Locate and identify every blood parasite.
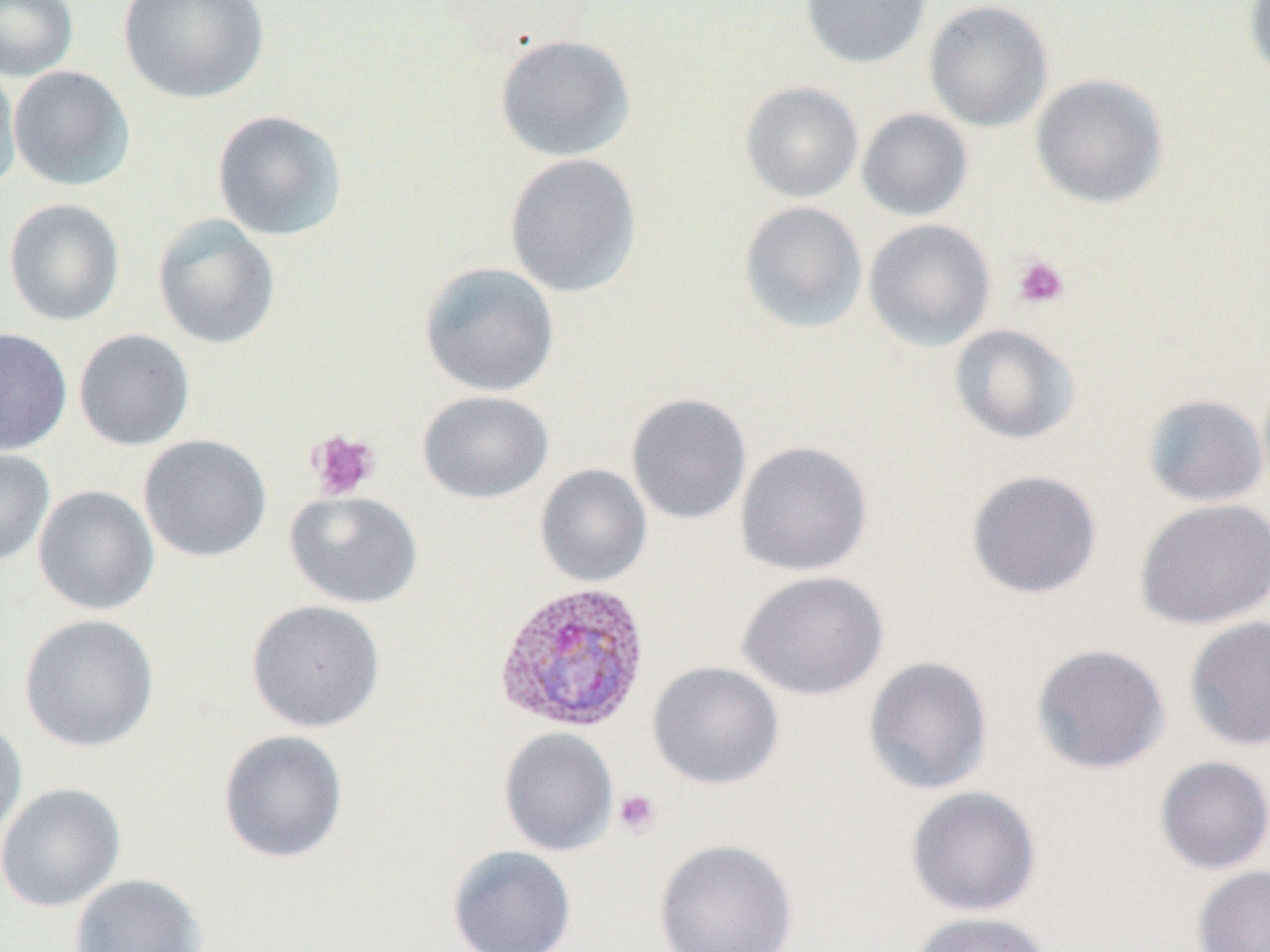
Approximate bounding boxes as named x1/y1/x2/y2 corners in pixels.
Plasmodium vivax-infected red blood cells: (x1=494, y1=581, x2=652, y2=733).
No Plasmodium falciparum, Plasmodium ovale, Plasmodium malariae, Babesia divergens, or Trypanosoma brucei observed.

slide_level_diagnosis: Plasmodium vivax
uninfected_red_blood_cell_locations: 'approximate bounding boxes as named x1/y1/x2/y2 corners in pixels: (x1=0, y1=0, x2=79, y2=81), (x1=118, y1=0, x2=269, y2=105), (x1=800, y1=0, x2=931, y2=69), (x1=923, y1=0, x2=1054, y2=132), (x1=1242, y1=0, x2=1270, y2=88), (x1=493, y1=33, x2=636, y2=162), (x1=0, y1=60, x2=21, y2=194), (x1=8, y1=66, x2=135, y2=191), (x1=1030, y1=73, x2=1168, y2=210), (x1=740, y1=82, x2=863, y2=202), (x1=856, y1=108, x2=973, y2=221), (x1=211, y1=109, x2=348, y2=242), (x1=504, y1=153, x2=642, y2=298), (x1=3, y1=198, x2=125, y2=327), (x1=738, y1=201, x2=868, y2=333), (x1=152, y1=213, x2=281, y2=350), (x1=864, y1=219, x2=996, y2=351), (x1=418, y1=261, x2=560, y2=397), (x1=949, y1=323, x2=1082, y2=445), (x1=0, y1=327, x2=72, y2=456), (x1=73, y1=329, x2=194, y2=451), (x1=416, y1=390, x2=553, y2=504), (x1=625, y1=393, x2=751, y2=525), (x1=1141, y1=393, x2=1269, y2=507), (x1=138, y1=434, x2=272, y2=563), (x1=735, y1=440, x2=873, y2=577), (x1=0, y1=448, x2=54, y2=568), (x1=535, y1=464, x2=652, y2=587), (x1=966, y1=469, x2=1103, y2=600), (x1=32, y1=485, x2=159, y2=616), (x1=284, y1=491, x2=424, y2=609), (x1=1134, y1=498, x2=1270, y2=631), (x1=737, y1=570, x2=888, y2=701), (x1=246, y1=599, x2=385, y2=733), (x1=18, y1=614, x2=159, y2=753), (x1=1184, y1=616, x2=1270, y2=752), (x1=1030, y1=642, x2=1171, y2=776), (x1=862, y1=655, x2=994, y2=796), (x1=647, y1=661, x2=784, y2=790), (x1=0, y1=717, x2=27, y2=844), (x1=499, y1=727, x2=618, y2=856), (x1=217, y1=729, x2=348, y2=864), (x1=1154, y1=755, x2=1270, y2=875), (x1=0, y1=782, x2=126, y2=912), (x1=905, y1=785, x2=1042, y2=917), (x1=653, y1=839, x2=798, y2=952), (x1=447, y1=845, x2=576, y2=952), (x1=1192, y1=865, x2=1270, y2=952), (x1=68, y1=873, x2=207, y2=952), (x1=907, y1=911, x2=1054, y2=952)'
modality: light microscopy
field_of_view: one of a larger specimen
stain: May-Grünwald-Giemsa
magnification: 1000x
platelet_locations: 'approximate bounding boxes as named x1/y1/x2/y2 corners in pixels: (x1=1012, y1=254, x2=1070, y2=309), (x1=306, y1=429, x2=380, y2=502), (x1=612, y1=789, x2=661, y2=839)'
image_size: 1270×952 pixels
preparation: thin blood film